Name the parasite shown.
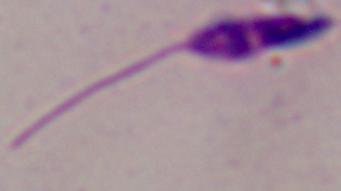

This is Leishmania.

Summary:
  - Modality: micrograph
  - Magnification: 1000x